Name the cell type shown.
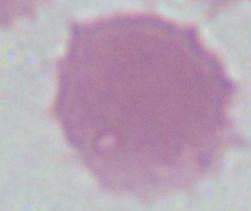
An erythrocyte.

{
  "magnification": "1000x",
  "modality": "photomicrograph"
}